Classify the preparation.
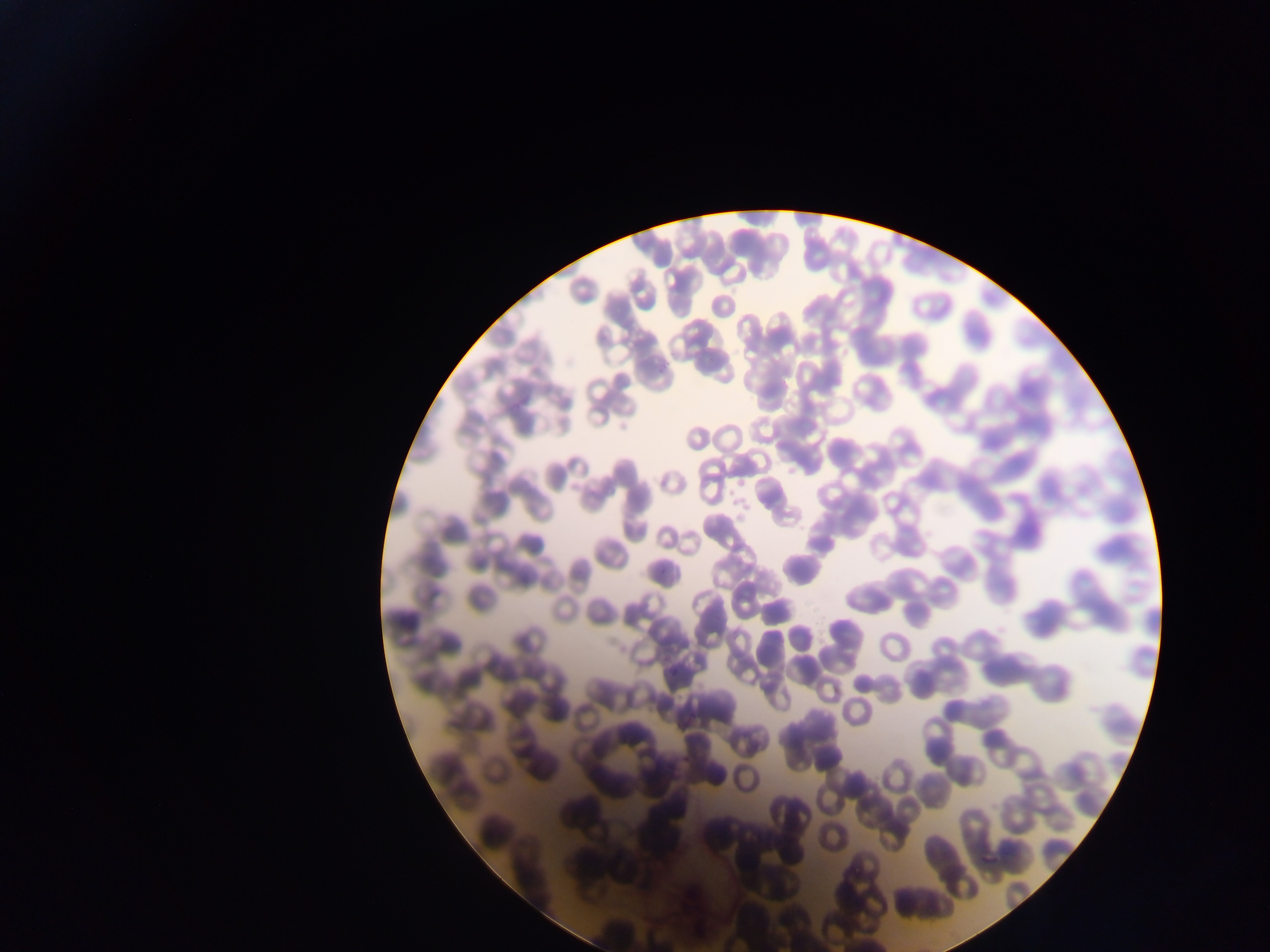

Thin blood film.

Approximate bounding boxes as left top right bottom in pixels. Malaria parasite locations: 708 354 715 364; 658 365 666 377; 660 560 671 572; 668 668 680 682; 687 708 699 719; 681 753 692 763. Image is 1270×952 pixels. Mobile-phone photograph taken through the microscope. Single field of view. Collected in Ghana.